Assess the morphology of the red blood cells.
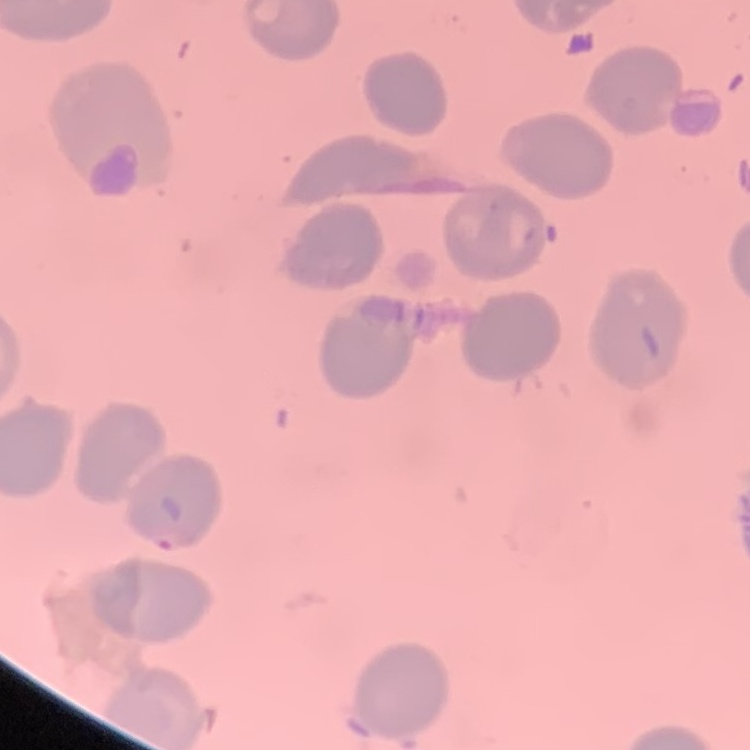

No rouleaux formation.

Field's or Giemsa stain. One tile cut from a larger photomicrograph. Thin blood film.